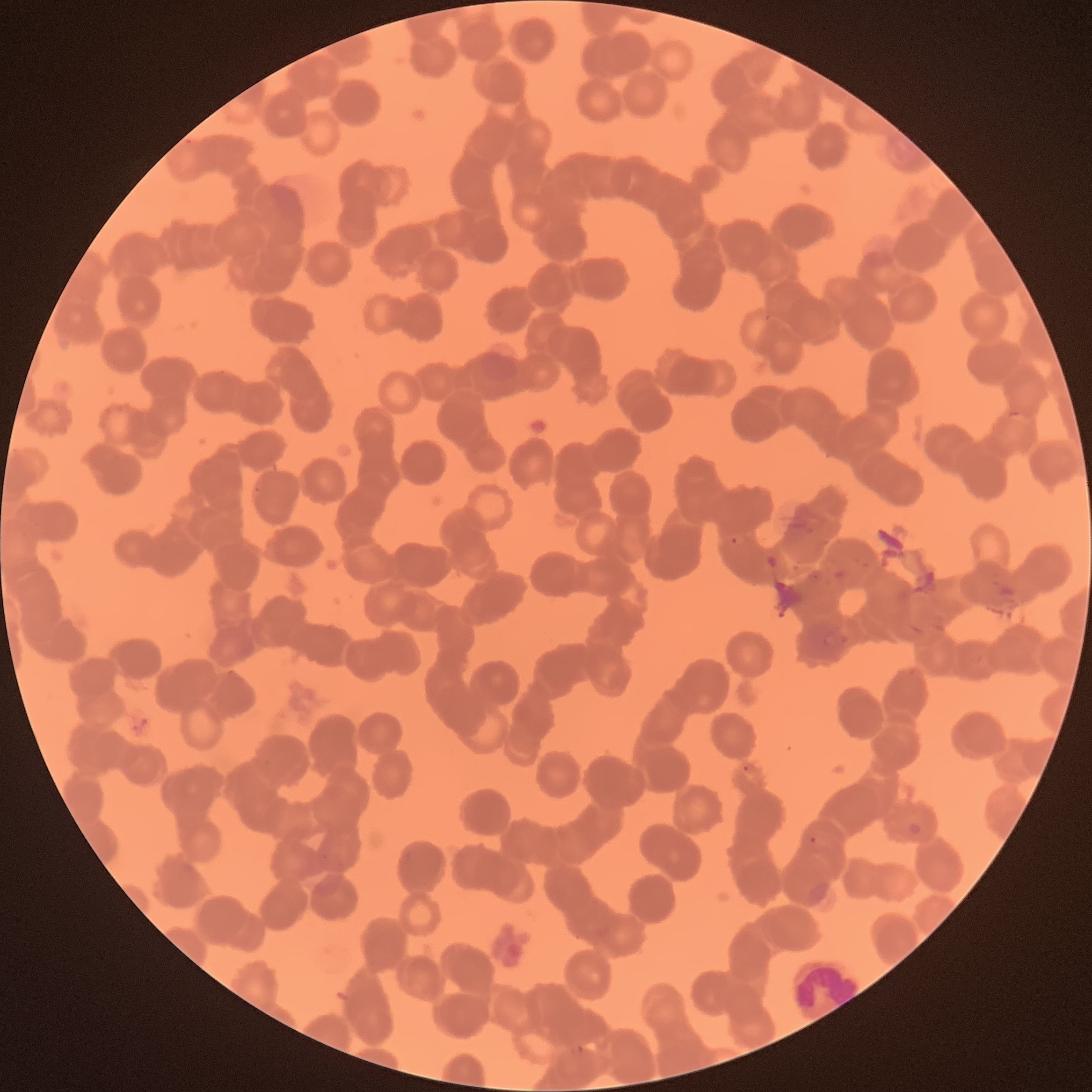

Approximate bounding boxes as (x1, y1, x2, y2) in pixels. Plasmodium parasite locations: (730, 536, 739, 544), (822, 630, 851, 650), (228, 669, 236, 676), (742, 764, 750, 772), (809, 835, 818, 845), (572, 1044, 587, 1055). White blood cell locations: (786, 960, 863, 1015). Plasmodium parasites too small for a box (approximate centers as (x, y) in pixels): (257, 490), (816, 577). The red blood cells show rouleaux formation. Image is 1092×1092 pixels. Thin blood film. Optical microscopy.